Assess this cell for malaria.
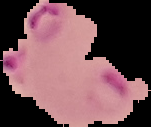
It is parasitized.

Summary:
  - Image size: 151×127 pixels
  - Preparation: thin blood smear
  - Image type: segmented cell region with the area outside set to black